Name the parasite shown.
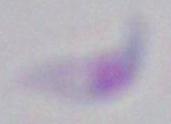

This is Toxoplasma gondii.

Summary:
  - Magnification: 1000x
  - Modality: photomicrograph